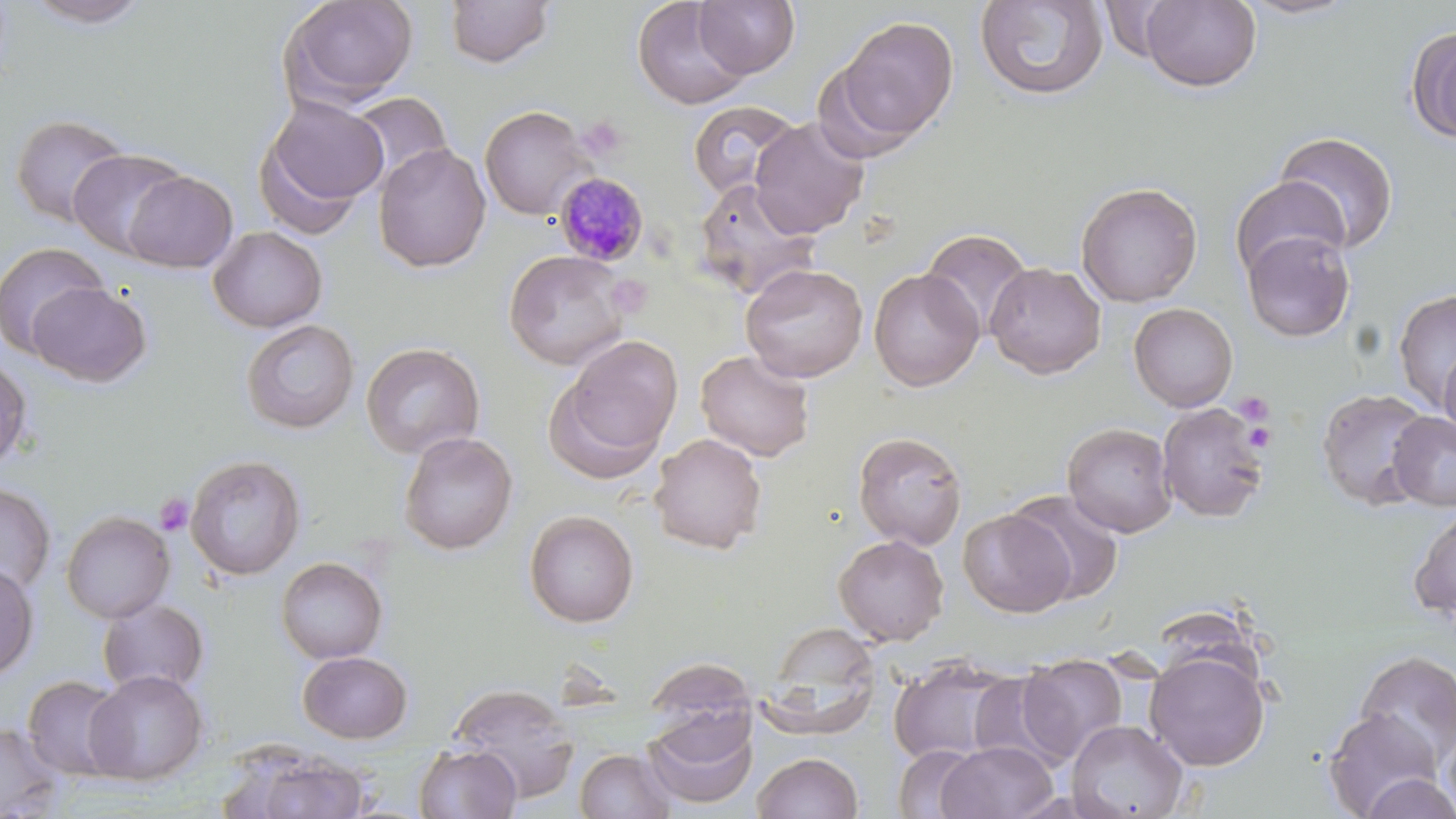
slide-level diagnosis = Plasmodium malariae
preparation = thin blood smear
platelet locations = approximate bounding boxes as named x1/y1/x2/y2 corners in pixels: (x1=575, y1=115, x2=629, y2=163), (x1=607, y1=273, x2=652, y2=317), (x1=1232, y1=392, x2=1274, y2=425), (x1=1244, y1=422, x2=1276, y2=452), (x1=154, y1=493, x2=193, y2=536)
modality = light microscopy
field of view = single
magnification = 1000x
Plasmodium malariae-infected red blood cell locations = approximate bounding boxes as named x1/y1/x2/y2 corners in pixels: (x1=555, y1=171, x2=649, y2=266)
image size = 1456×819 pixels
stain = May-Grünwald-Giemsa
uninfected red blood cell locations = approximate bounding boxes as named x1/y1/x2/y2 corners in pixels: (x1=20, y1=0, x2=155, y2=29), (x1=279, y1=0, x2=419, y2=110), (x1=632, y1=0, x2=753, y2=111), (x1=694, y1=0, x2=800, y2=78), (x1=975, y1=0, x2=1108, y2=101), (x1=1233, y1=0, x2=1364, y2=21), (x1=444, y1=1, x2=555, y2=68), (x1=1139, y1=1, x2=1262, y2=92), (x1=835, y1=15, x2=958, y2=145), (x1=1406, y1=24, x2=1456, y2=145), (x1=348, y1=91, x2=454, y2=192), (x1=256, y1=95, x2=389, y2=229), (x1=687, y1=100, x2=802, y2=201), (x1=479, y1=105, x2=595, y2=221), (x1=10, y1=113, x2=132, y2=229), (x1=749, y1=117, x2=869, y2=239), (x1=1273, y1=131, x2=1400, y2=253), (x1=373, y1=143, x2=491, y2=273), (x1=68, y1=148, x2=190, y2=258), (x1=122, y1=170, x2=238, y2=273), (x1=1228, y1=175, x2=1351, y2=283), (x1=693, y1=178, x2=819, y2=300), (x1=1076, y1=181, x2=1203, y2=307), (x1=207, y1=226, x2=327, y2=333), (x1=920, y1=228, x2=1033, y2=341), (x1=1241, y1=229, x2=1356, y2=342), (x1=0, y1=241, x2=110, y2=358), (x1=503, y1=249, x2=631, y2=371), (x1=985, y1=262, x2=1106, y2=379), (x1=739, y1=263, x2=868, y2=382), (x1=868, y1=268, x2=984, y2=391), (x1=28, y1=281, x2=152, y2=387), (x1=1392, y1=288, x2=1456, y2=413), (x1=1128, y1=303, x2=1238, y2=412), (x1=240, y1=319, x2=360, y2=434), (x1=554, y1=333, x2=683, y2=472), (x1=361, y1=342, x2=485, y2=459), (x1=1439, y1=343, x2=1456, y2=450), (x1=695, y1=350, x2=815, y2=462), (x1=0, y1=354, x2=32, y2=473), (x1=1316, y1=388, x2=1433, y2=510), (x1=1157, y1=403, x2=1269, y2=523), (x1=1387, y1=411, x2=1456, y2=511), (x1=1062, y1=422, x2=1177, y2=538), (x1=398, y1=431, x2=518, y2=555), (x1=853, y1=431, x2=968, y2=550), (x1=649, y1=433, x2=767, y2=554), (x1=185, y1=454, x2=306, y2=580), (x1=0, y1=482, x2=57, y2=598), (x1=1008, y1=490, x2=1125, y2=605), (x1=1409, y1=505, x2=1456, y2=621), (x1=958, y1=508, x2=1076, y2=617), (x1=523, y1=509, x2=639, y2=628), (x1=61, y1=510, x2=176, y2=623), (x1=833, y1=534, x2=949, y2=646), (x1=276, y1=556, x2=388, y2=664), (x1=0, y1=562, x2=39, y2=681), (x1=96, y1=598, x2=210, y2=698), (x1=1145, y1=650, x2=1270, y2=771), (x1=1352, y1=650, x2=1456, y2=769), (x1=298, y1=651, x2=413, y2=743), (x1=1018, y1=653, x2=1128, y2=764), (x1=645, y1=655, x2=756, y2=737), (x1=887, y1=656, x2=1019, y2=767), (x1=83, y1=670, x2=208, y2=785), (x1=968, y1=670, x2=1073, y2=773), (x1=22, y1=675, x2=130, y2=782), (x1=448, y1=682, x2=580, y2=802), (x1=644, y1=709, x2=758, y2=810), (x1=1323, y1=709, x2=1445, y2=818), (x1=1439, y1=718, x2=1456, y2=818), (x1=1066, y1=719, x2=1188, y2=819), (x1=0, y1=721, x2=65, y2=817), (x1=936, y1=741, x2=1058, y2=819), (x1=415, y1=744, x2=521, y2=819), (x1=893, y1=745, x2=984, y2=819), (x1=575, y1=748, x2=677, y2=819), (x1=752, y1=752, x2=863, y2=818), (x1=250, y1=753, x2=371, y2=819), (x1=1358, y1=773, x2=1455, y2=818)